Assess this cell for malaria.
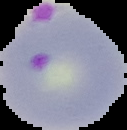
It is parasitized.

Summary:
  - Image size: 127×130 pixels
  - Image type: cell region segmented out of the field of view; surrounding area masked to black
  - Preparation: thin blood film